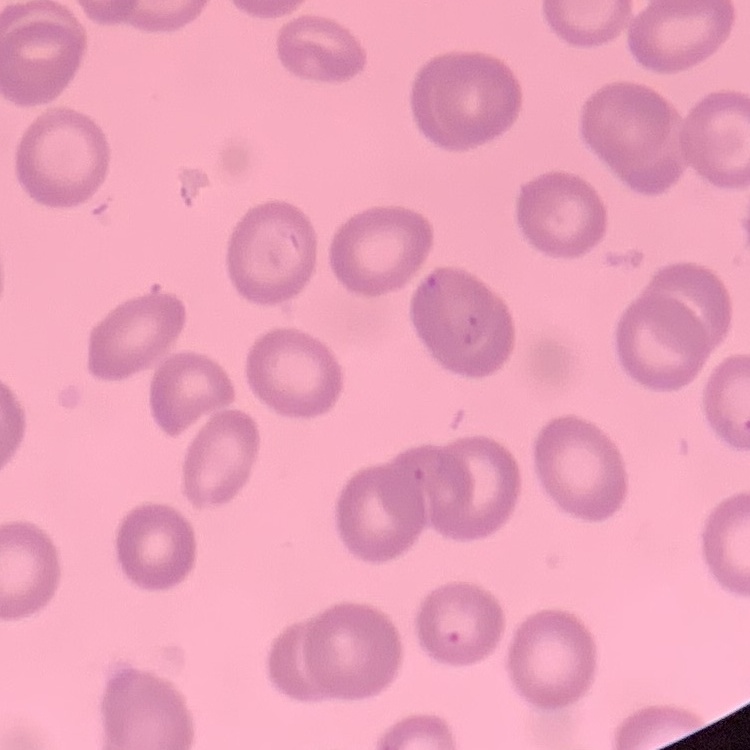
The erythrocytes exhibit no rouleaux formation. Thin blood film. Stained with either Field's or Giemsa. Square crop of a larger photomicrograph.